Locate every blood parasite and identify its species.
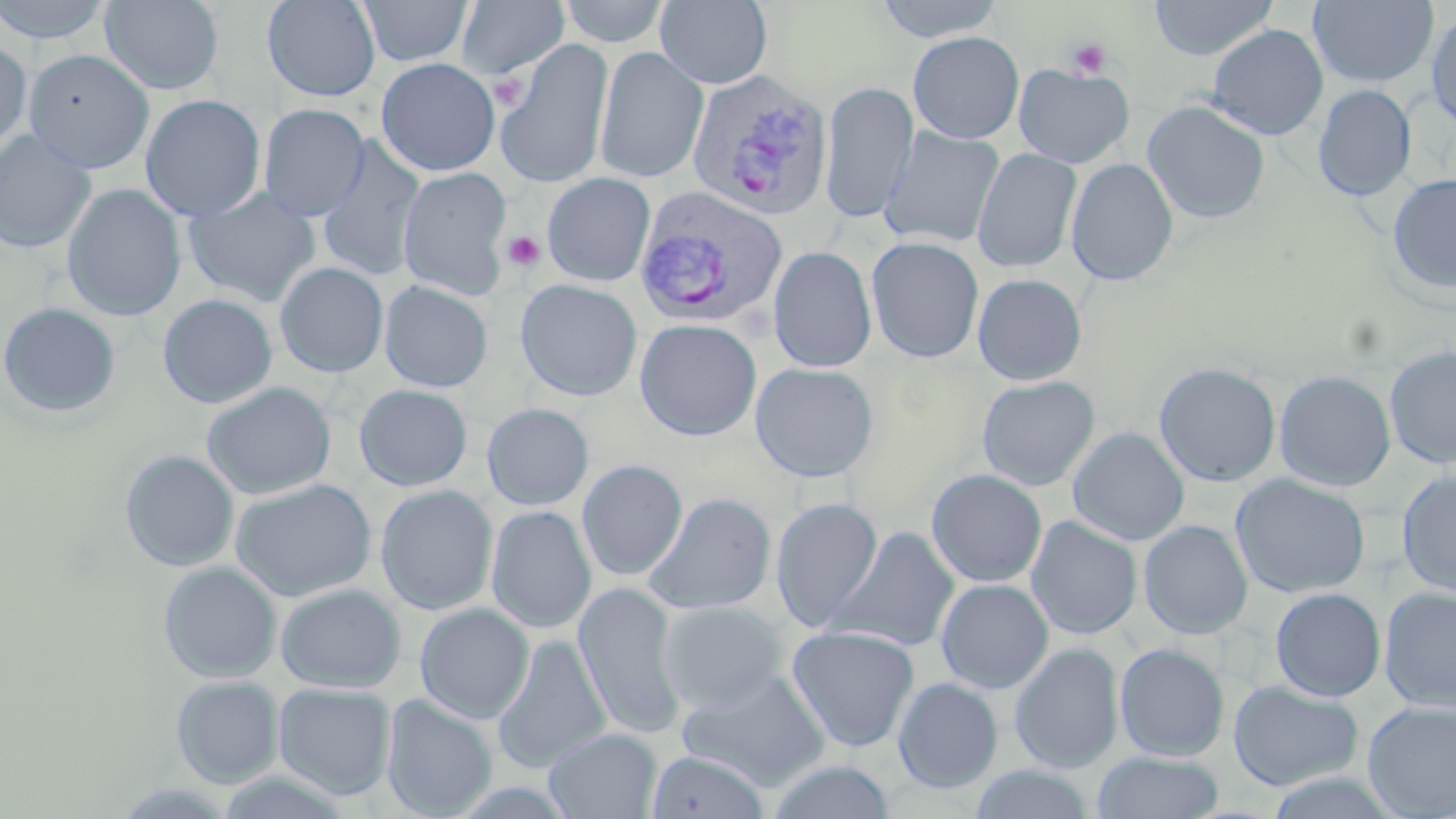
Approximate bounding boxes as [x1, y1, x2, y2] in pixels.
Plasmodium vivax-infected red blood cells: [685, 69, 832, 222], [634, 186, 789, 330].
No Plasmodium falciparum, Plasmodium ovale, Plasmodium malariae, Babesia divergens, or Trypanosoma brucei observed.

slide-level diagnosis = Plasmodium vivax
field of view = single
image size = 1456×819 pixels
stain = May-Grünwald-Giemsa
modality = optical microscopy
platelet locations = approximate bounding boxes as [x1, y1, x2, y2] in pixels: [1067, 38, 1111, 79], [489, 74, 526, 109], [502, 231, 545, 273]
uninfected red blood cell locations = approximate bounding boxes as [x1, y1, x2, y2] in pixels: [0, 0, 115, 44], [100, 0, 223, 95], [262, 0, 380, 102], [357, 0, 474, 67], [559, 0, 670, 47], [655, 0, 772, 88], [874, 0, 1004, 43], [1148, 0, 1278, 61], [456, 1, 569, 80], [1308, 1, 1438, 88], [1426, 9, 1456, 132], [1206, 24, 1329, 140], [908, 31, 1025, 144], [495, 38, 614, 189], [0, 41, 32, 154], [594, 47, 708, 183], [24, 49, 154, 172], [376, 58, 500, 176], [1013, 63, 1134, 167], [820, 82, 918, 223], [1312, 84, 1416, 201], [140, 94, 265, 221], [1142, 100, 1271, 225], [258, 104, 369, 221], [879, 126, 1004, 249], [0, 130, 96, 254], [316, 138, 427, 282], [971, 148, 1082, 272], [1066, 158, 1179, 286], [398, 167, 512, 300], [1386, 172, 1456, 296], [542, 173, 655, 286], [62, 184, 185, 321], [183, 188, 321, 307], [866, 236, 984, 362], [768, 245, 876, 372], [275, 262, 388, 377], [972, 273, 1087, 385], [515, 279, 642, 401], [379, 280, 493, 393], [158, 294, 278, 409], [0, 302, 121, 419], [635, 318, 762, 440], [1384, 344, 1456, 470], [750, 362, 879, 482], [1154, 362, 1281, 487], [1274, 370, 1396, 491], [977, 375, 1099, 491], [201, 381, 336, 500], [354, 384, 472, 491], [482, 403, 593, 510], [1068, 427, 1189, 545], [119, 449, 239, 572], [577, 459, 687, 581], [927, 469, 1047, 587], [1396, 470, 1456, 597], [1231, 474, 1370, 598], [230, 478, 376, 601], [375, 485, 498, 615], [644, 493, 775, 615], [770, 497, 883, 632], [486, 505, 596, 633], [1026, 516, 1142, 639], [1139, 520, 1253, 639], [829, 526, 960, 652], [158, 561, 282, 683], [936, 579, 1053, 693], [274, 583, 406, 693], [573, 583, 686, 740], [1379, 586, 1456, 713], [1270, 587, 1385, 701], [659, 601, 788, 712], [414, 604, 534, 723], [786, 624, 919, 752], [492, 634, 611, 773], [1009, 642, 1124, 773], [1114, 642, 1230, 762], [678, 669, 830, 791], [170, 675, 284, 788], [507, 675, 650, 814], [893, 678, 1003, 793], [1228, 680, 1363, 792], [273, 683, 396, 800], [382, 695, 497, 817], [1362, 701, 1456, 817], [544, 727, 662, 819], [646, 750, 769, 819], [1091, 751, 1224, 819], [765, 760, 896, 819], [967, 765, 1097, 819]
preparation = thin blood smear
magnification = 1000x